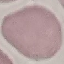 Malaria status: uninfected. Cell patch, automatically extracted from a larger field of view and resized to 64 × 64 pixels. Photographed with a smartphone camera at the microscope eyepiece. Giemsa stain. Thin blood smear.